Identify the cell.
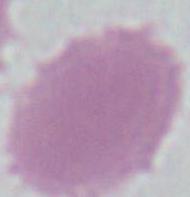
An erythrocyte.

magnification: 1000x
modality: photomicrograph